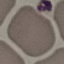
malaria status = uninfected
stain = Giemsa
capture = smartphone camera at the microscope eyepiece
image type = automatically extracted cell patch, resized to 64 × 64 pixels
preparation = thin blood film